Assess this cell for malaria.
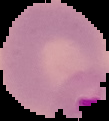

Parasitized.

Summary:
  - Image size: 109×121 pixels
  - Preparation: thin blood smear
  - Image type: cell region segmented out of the field of view; surrounding area masked to black